Assess the morphology of the red blood cells.
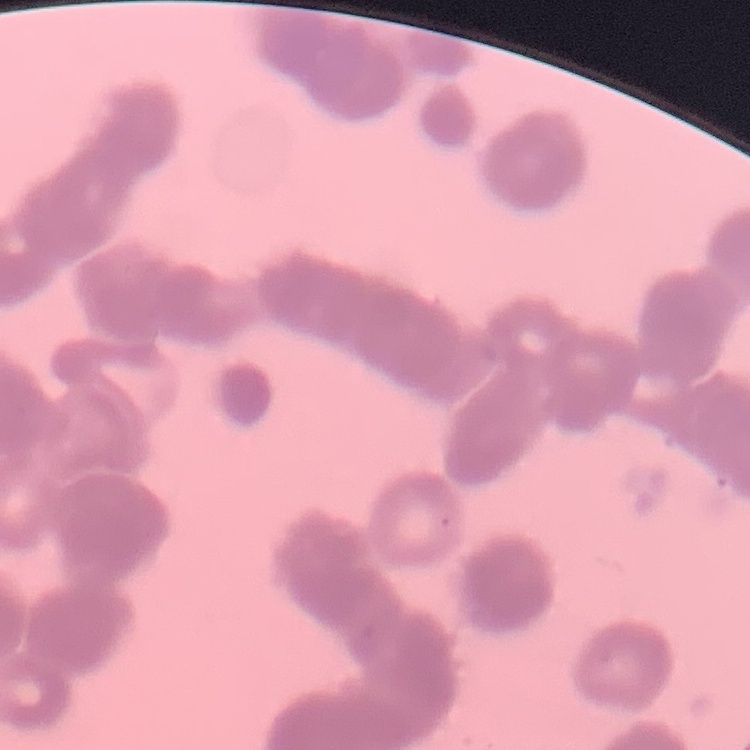

They show rouleaux formation.

Square crop of a larger photomicrograph. Thin blood film. Stained with either Field's or Giemsa.